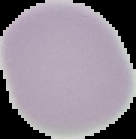

Summary:
  - Preparation: thin blood film
  - Result: no Plasmodium parasites seen
  - Image type: cell region segmented out of the field of view; surrounding area masked to black
  - Image size: 136×139 pixels